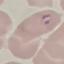

result = malaria parasites identified
capture = smartphone through the microscope eyepiece
image type = cell patch, automatically extracted from a larger field of view and resized to 64 × 64 pixels
preparation = thin smear
stain = Giemsa